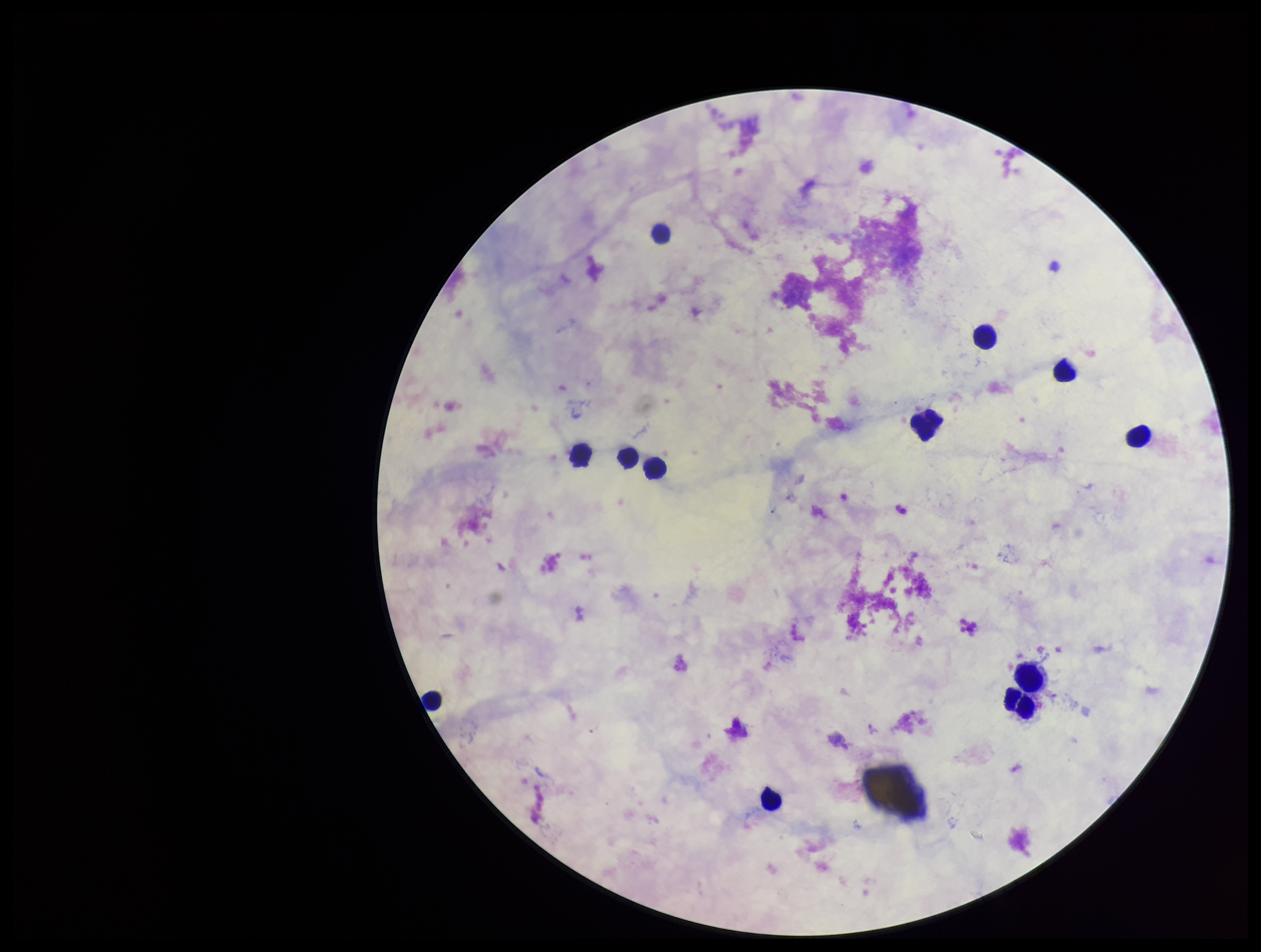 Single field of view. Stained with Giemsa. Plasmodium parasites: none seen. Patient malaria status: negative. Leukocyte count: 12. Parasite count: 0. Preparation: thick blood smear. Image is 1261×952 pixels. Photographed through the microscope eyepiece with a smartphone camera.